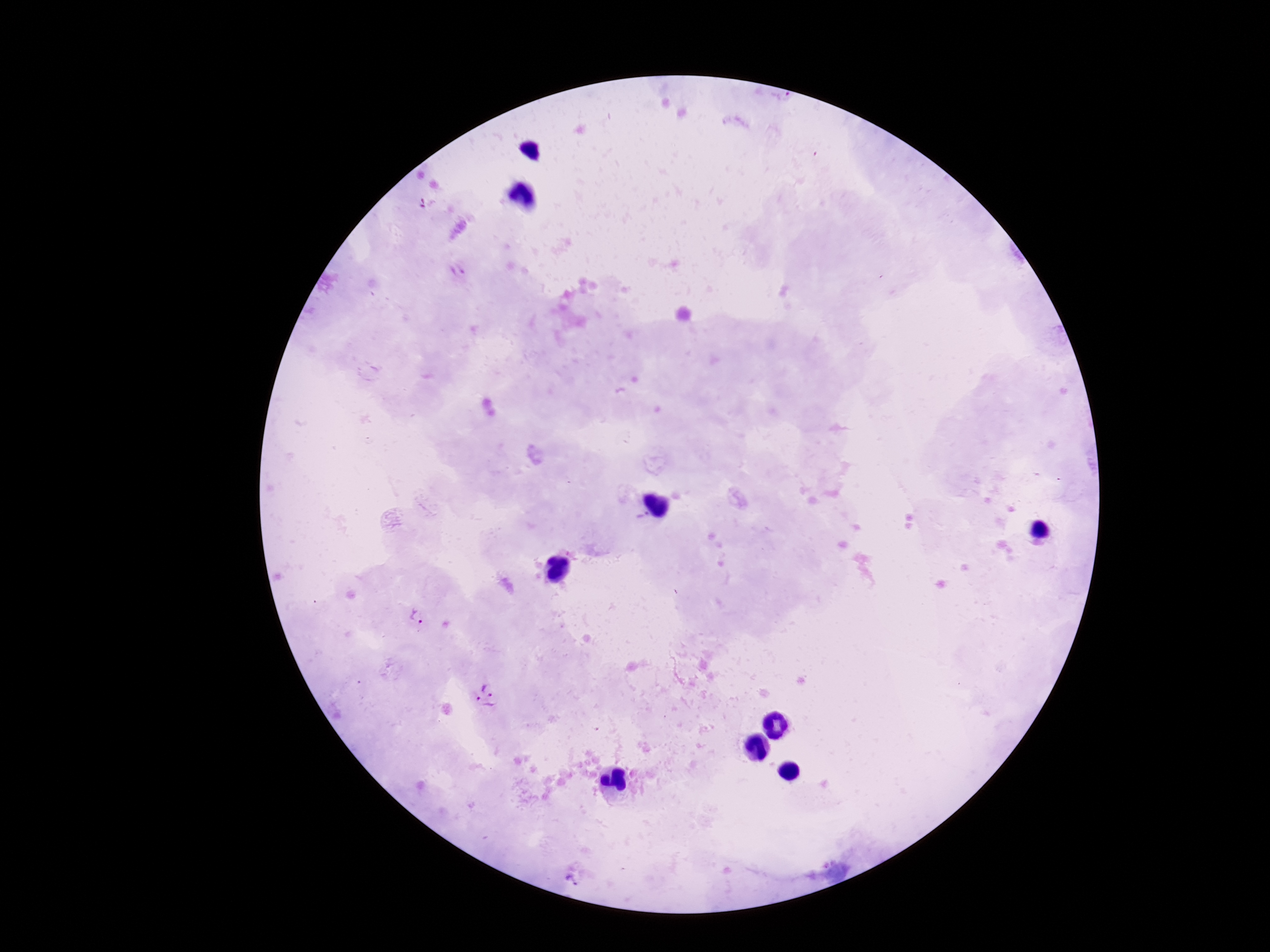
field of view = one from this slide
Plasmodium parasite locations = approximate centers as {x, y} in pixels: {458, 271}, {414, 618}, {489, 684}, {483, 710}, {570, 878}
preparation = thick blood film
patient malaria status = positive
capture = smartphone camera through the microscope eyepiece
magnification = 100x
stain = Giemsa
image size = 1270×952 pixels